Outline each uninfected red blood cell.
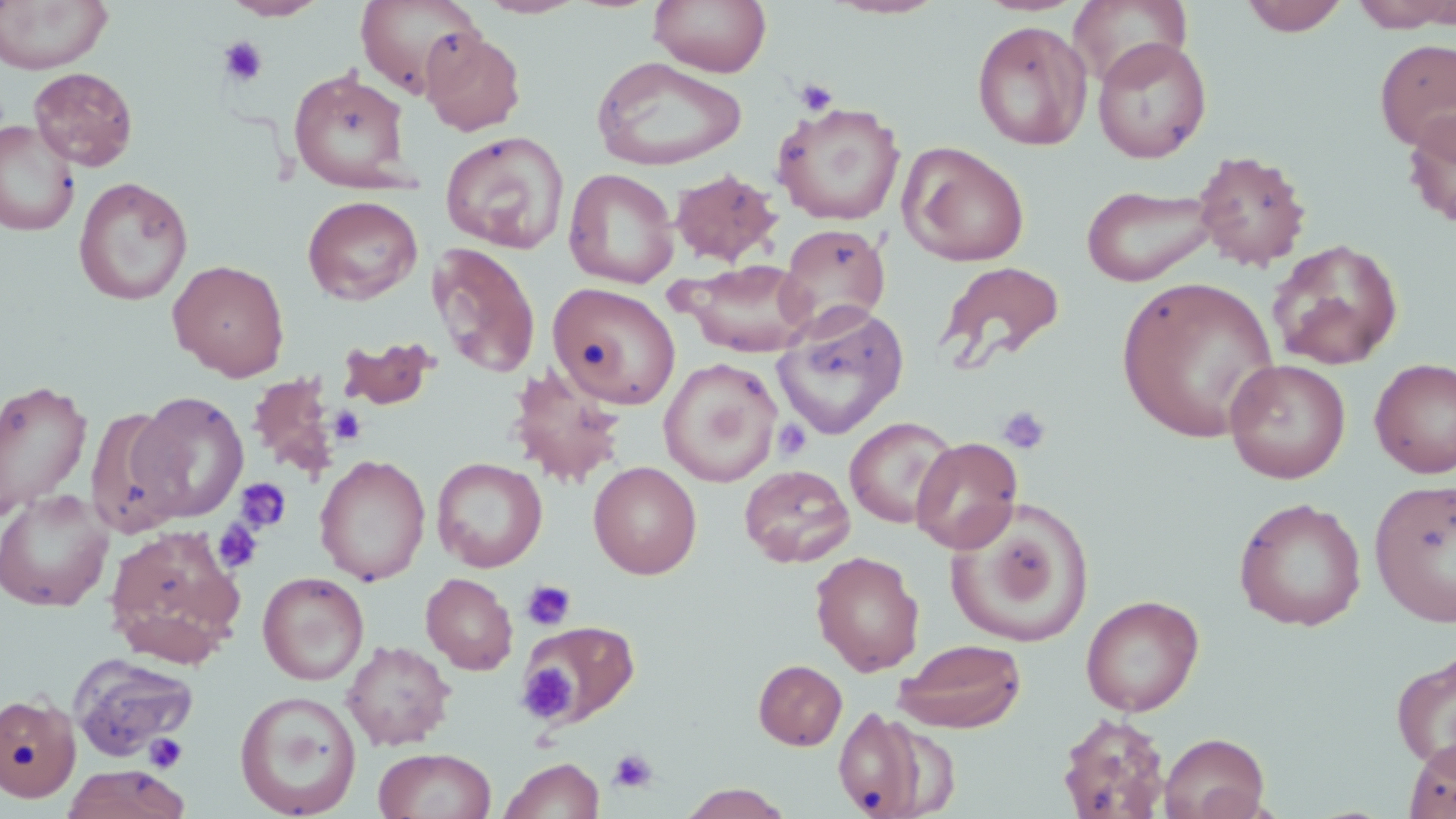

Approximate bounding boxes as named x1/y1/x2/y2 corners in pixels.
Uninfected red blood cells: (x1=0, y1=0, x2=114, y2=74), (x1=222, y1=0, x2=330, y2=21), (x1=355, y1=0, x2=484, y2=98), (x1=476, y1=0, x2=588, y2=19), (x1=650, y1=0, x2=771, y2=77), (x1=823, y1=0, x2=948, y2=20), (x1=1068, y1=0, x2=1193, y2=87), (x1=1240, y1=0, x2=1349, y2=36), (x1=1350, y1=0, x2=1456, y2=31), (x1=972, y1=20, x2=1093, y2=150), (x1=421, y1=29, x2=527, y2=136), (x1=1091, y1=36, x2=1212, y2=163), (x1=1375, y1=38, x2=1456, y2=154), (x1=591, y1=55, x2=747, y2=171), (x1=28, y1=67, x2=138, y2=171), (x1=288, y1=67, x2=412, y2=192), (x1=773, y1=102, x2=905, y2=226), (x1=1402, y1=106, x2=1456, y2=230), (x1=0, y1=120, x2=79, y2=236), (x1=440, y1=130, x2=569, y2=253), (x1=898, y1=141, x2=1030, y2=266), (x1=1192, y1=149, x2=1311, y2=271), (x1=563, y1=168, x2=679, y2=289), (x1=670, y1=169, x2=782, y2=266), (x1=74, y1=177, x2=193, y2=305), (x1=1080, y1=182, x2=1221, y2=287), (x1=302, y1=195, x2=422, y2=305), (x1=776, y1=223, x2=890, y2=337), (x1=1268, y1=238, x2=1404, y2=370), (x1=427, y1=243, x2=541, y2=380), (x1=676, y1=258, x2=817, y2=357), (x1=168, y1=259, x2=290, y2=381), (x1=936, y1=261, x2=1066, y2=371), (x1=1117, y1=277, x2=1280, y2=443), (x1=548, y1=282, x2=681, y2=409), (x1=771, y1=303, x2=909, y2=440), (x1=337, y1=335, x2=442, y2=411), (x1=1369, y1=357, x2=1456, y2=479), (x1=659, y1=359, x2=782, y2=486), (x1=1224, y1=359, x2=1351, y2=484), (x1=507, y1=364, x2=629, y2=489), (x1=248, y1=374, x2=343, y2=481), (x1=0, y1=380, x2=92, y2=517), (x1=131, y1=392, x2=248, y2=523), (x1=86, y1=406, x2=189, y2=537), (x1=844, y1=416, x2=958, y2=529), (x1=911, y1=436, x2=1023, y2=554), (x1=314, y1=454, x2=431, y2=586), (x1=432, y1=457, x2=548, y2=572), (x1=588, y1=461, x2=702, y2=579), (x1=739, y1=464, x2=854, y2=567), (x1=1370, y1=479, x2=1456, y2=628), (x1=0, y1=489, x2=115, y2=612), (x1=1233, y1=497, x2=1367, y2=631), (x1=947, y1=506, x2=1092, y2=648), (x1=104, y1=524, x2=246, y2=667), (x1=810, y1=551, x2=924, y2=676), (x1=258, y1=571, x2=369, y2=685), (x1=421, y1=572, x2=518, y2=675), (x1=1081, y1=594, x2=1204, y2=716), (x1=518, y1=620, x2=639, y2=728), (x1=894, y1=638, x2=1026, y2=733), (x1=342, y1=640, x2=455, y2=750), (x1=1391, y1=650, x2=1456, y2=773), (x1=68, y1=654, x2=198, y2=760), (x1=753, y1=660, x2=847, y2=750), (x1=235, y1=690, x2=362, y2=818), (x1=0, y1=692, x2=81, y2=803), (x1=832, y1=705, x2=953, y2=818), (x1=1056, y1=713, x2=1172, y2=818), (x1=1159, y1=732, x2=1270, y2=819), (x1=1403, y1=737, x2=1456, y2=818), (x1=373, y1=747, x2=496, y2=819), (x1=499, y1=757, x2=605, y2=818), (x1=61, y1=764, x2=191, y2=819), (x1=678, y1=783, x2=794, y2=818).

slide_level_diagnosis: negative for blood parasites
field_of_view: one of a larger specimen
modality: light microscopy
stain: May-Grünwald-Giemsa
magnification: 1000x
image_size: 1456×819 pixels
preparation: thin blood smear
platelet_locations: 'approximate bounding boxes as named x1/y1/x2/y2 corners in pixels: (x1=218, y1=36, x2=268, y2=86), (x1=795, y1=78, x2=839, y2=116), (x1=997, y1=404, x2=1052, y2=456), (x1=328, y1=406, x2=366, y2=445), (x1=773, y1=418, x2=812, y2=461), (x1=235, y1=478, x2=291, y2=534), (x1=212, y1=519, x2=264, y2=574), (x1=521, y1=580, x2=576, y2=631), (x1=518, y1=664, x2=578, y2=721), (x1=144, y1=732, x2=188, y2=773), (x1=609, y1=748, x2=658, y2=794)'